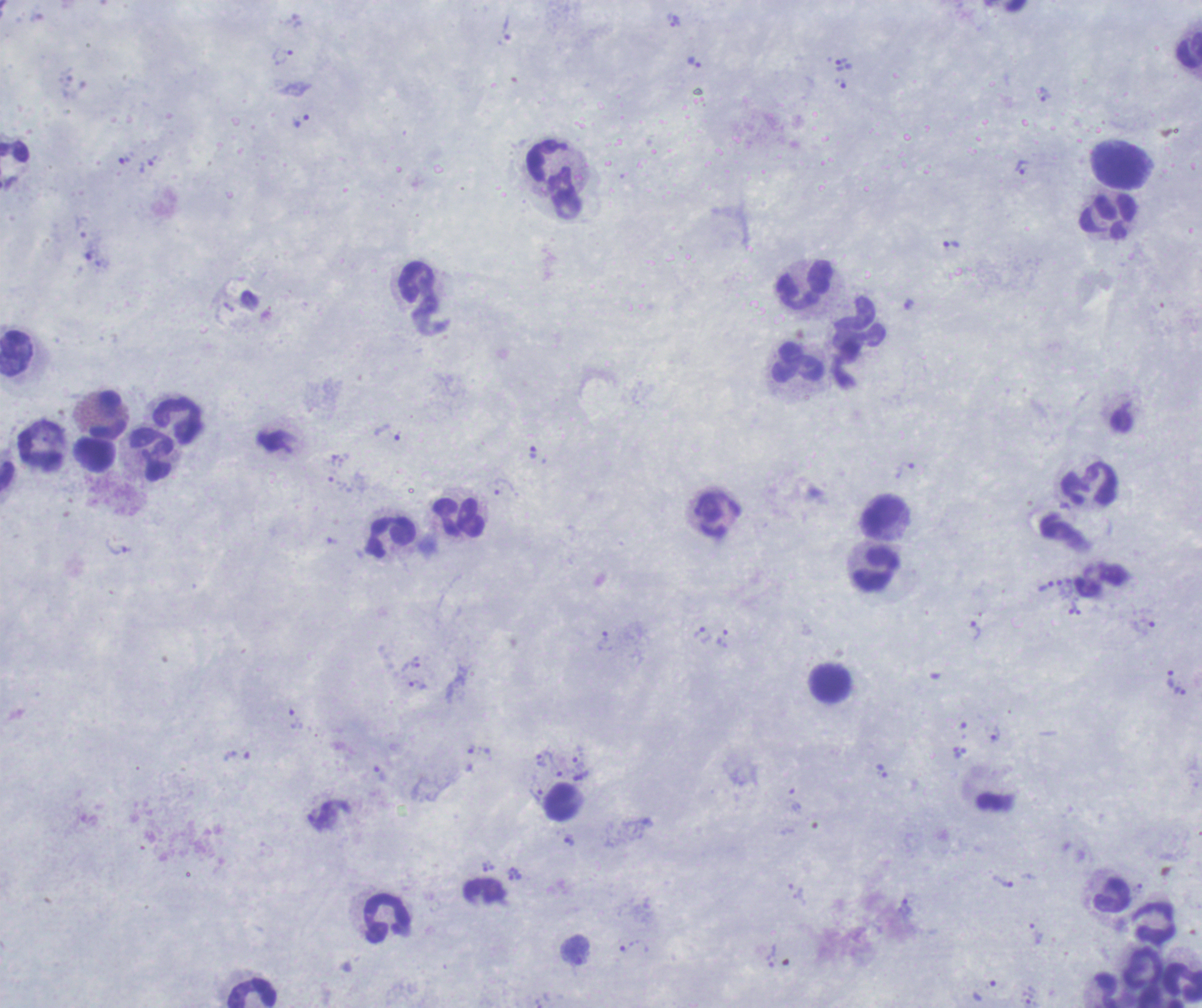

Thick blood film. Romanowsky-stained preparation. One field from this slide. Image is 1202×1008 pixels.